Assess this cell for malaria.
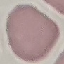
It is uninfected.

Automatically extracted cell patch, resized to 64 × 64 pixels. Thin blood film. Giemsa-stained preparation. Acquired by smartphone through the microscope eyepiece.